Identify the parasite.
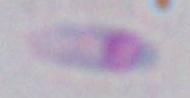
This is Toxoplasma gondii.

Summary:
  - Magnification: 1000x
  - Modality: micrograph